Give a bounding box for every leukocyte visible.
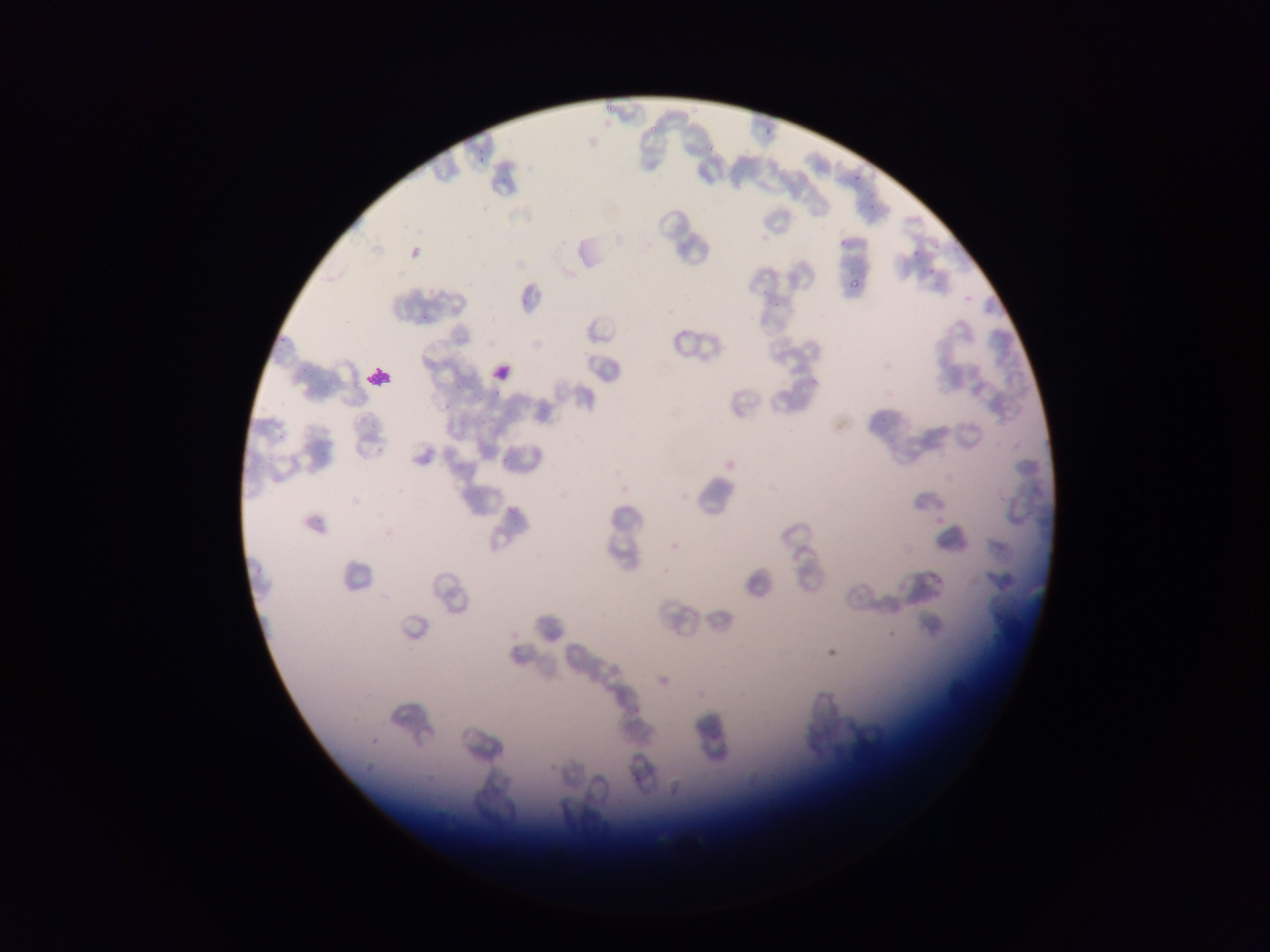

Approximate bounding boxes as (left, top, right, bottom) in pixels.
Leukocytes: (490, 363, 513, 383), (367, 368, 395, 387).

{
  "field_of_view": "single",
  "image_size": "1270×952 pixels",
  "preparation": "thin blood smear",
  "capture": "mobile-phone photograph through a microscope",
  "plasmodium_parasite_locations": "approximate bounding boxes as (left, top, right, bottom) in pixels: (605, 103, 614, 114), (648, 123, 659, 133), (762, 125, 775, 137), (476, 156, 491, 164), (866, 191, 877, 197), (837, 237, 845, 246), (912, 249, 920, 255), (927, 262, 938, 275), (848, 279, 863, 289), (809, 373, 818, 384), (354, 380, 362, 388), (369, 417, 383, 427), (508, 505, 518, 514), (996, 580, 1005, 592) | approximate (x, y) pixel centers of objects too small to bound: (856, 178)",
  "country": "Ghana"
}